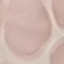
Result: no malaria parasites seen. Photographed with a smartphone camera at the microscope eyepiece. Thin smear of blood. Automatically extracted cell patch, resized to 64 × 64 pixels. Giemsa stain.